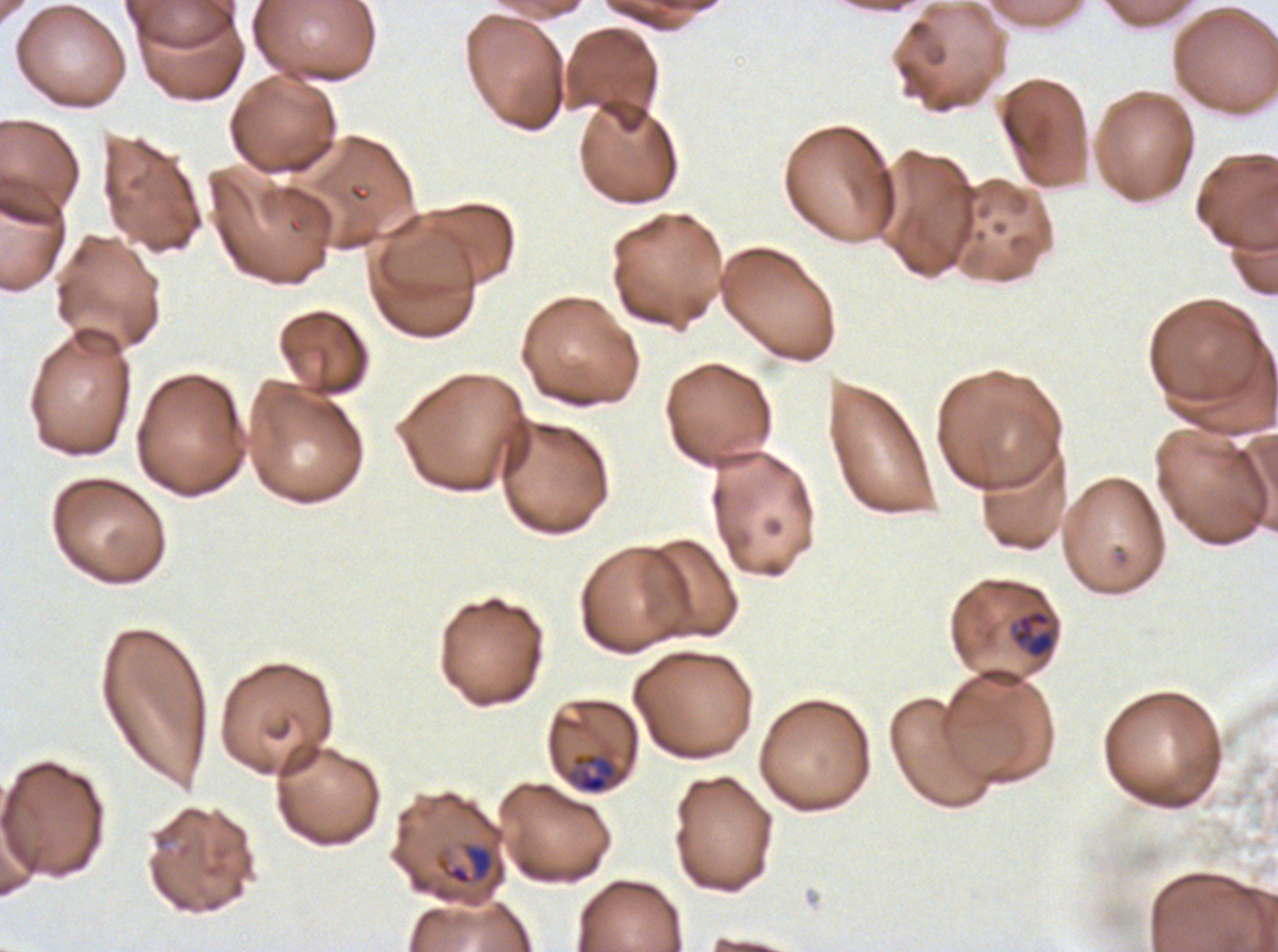

Approximate bounding rectangles given as corner coordinates in pixels from the top-left. Late-ring/early-trophozoite locations: (x1=1011, y1=608, x2=1056, y2=660). Mid trophozoite locations: (x1=567, y1=752, x2=619, y2=795), (x1=445, y1=843, x2=495, y2=885). One sub-image of a larger composite. Life-cycle stages observed: late-ring/early-trophozoite, mid trophozoite. Thin blood film. Plasmodium falciparum cultured ex vivo for 24 to 48 hours, from a patient in The Gambia. Giemsa stain. Image is 1278×952 pixels.